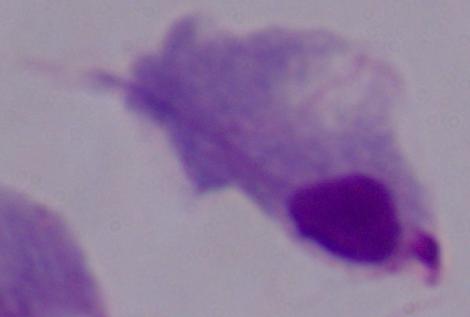
modality: photomicrograph
identification: trichomonad
magnification: 1000x